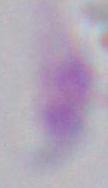
Summary:
  - Modality: micrograph
  - Magnification: 1000x
  - Identification: Toxoplasma gondii